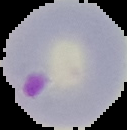

image type = segmented cell region with the area outside set to black
preparation = thin blood smear
malaria status = parasitized
image size = 127×130 pixels